Classify the preparation.
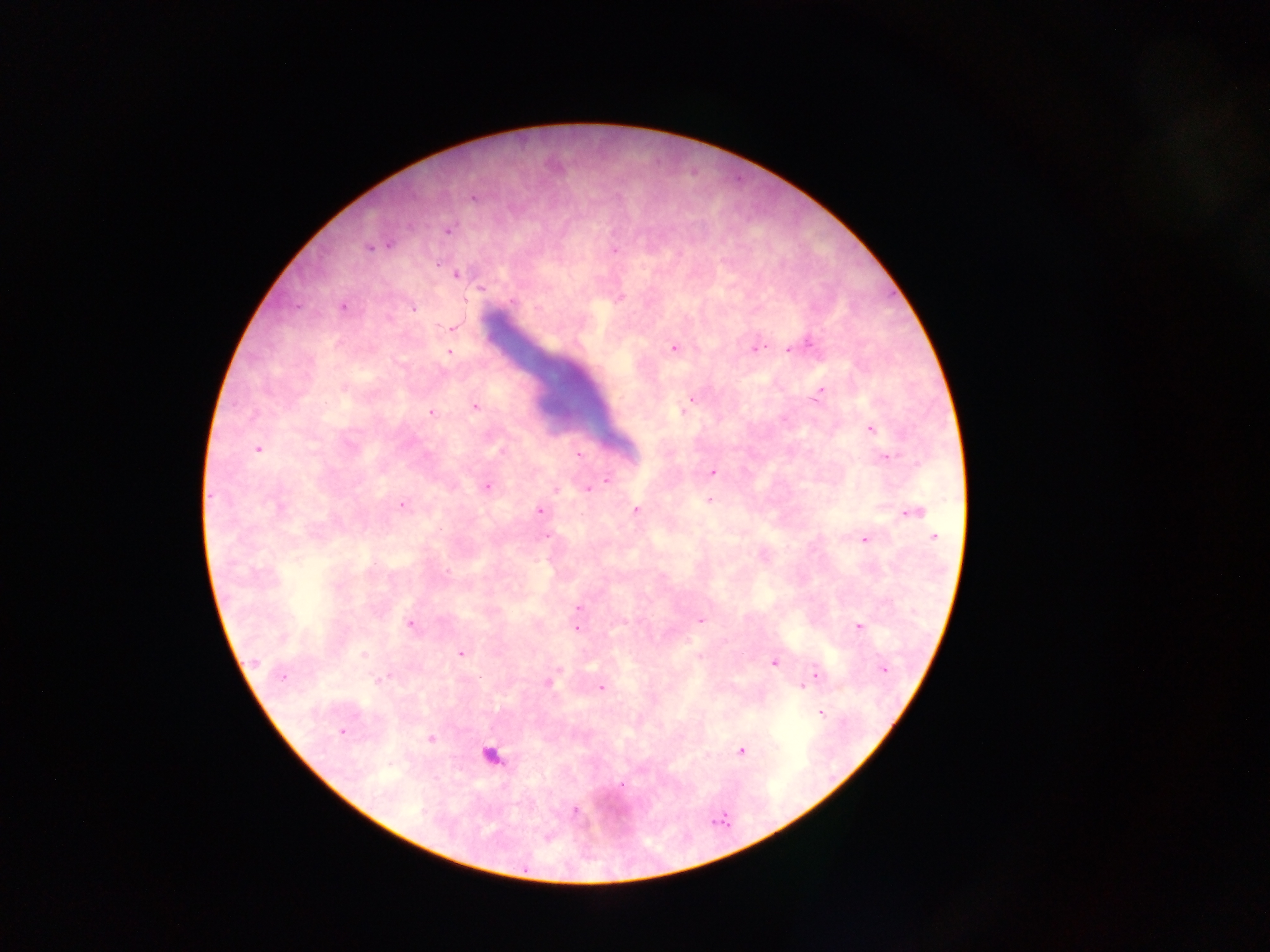

Thick blood film.

capture = mobile-phone photograph through a microscope
Plasmodium parasite locations = approximate centers as (x, y) in pixels: (473, 198), (447, 230), (369, 247), (614, 250), (457, 274), (620, 297), (343, 306), (412, 307), (451, 327), (802, 345), (674, 347), (792, 347), (755, 348), (449, 353), (817, 394), (691, 398), (475, 407), (431, 413), (870, 428), (257, 448), (576, 455), (885, 456), (712, 471), (607, 480), (486, 486), (588, 488), (709, 499), (402, 504), (540, 510), (636, 510), (913, 511), (933, 537), (864, 539), (578, 608), (700, 620), (409, 623), (858, 627), (575, 628), (461, 653), (774, 662), (883, 669), (815, 675), (282, 676), (548, 681), (807, 681), (803, 686), (601, 687), (821, 712), (343, 732), (431, 738), (741, 750), (490, 755), (574, 810)
field of view = single
country = Ghana
image size = 1270×952 pixels